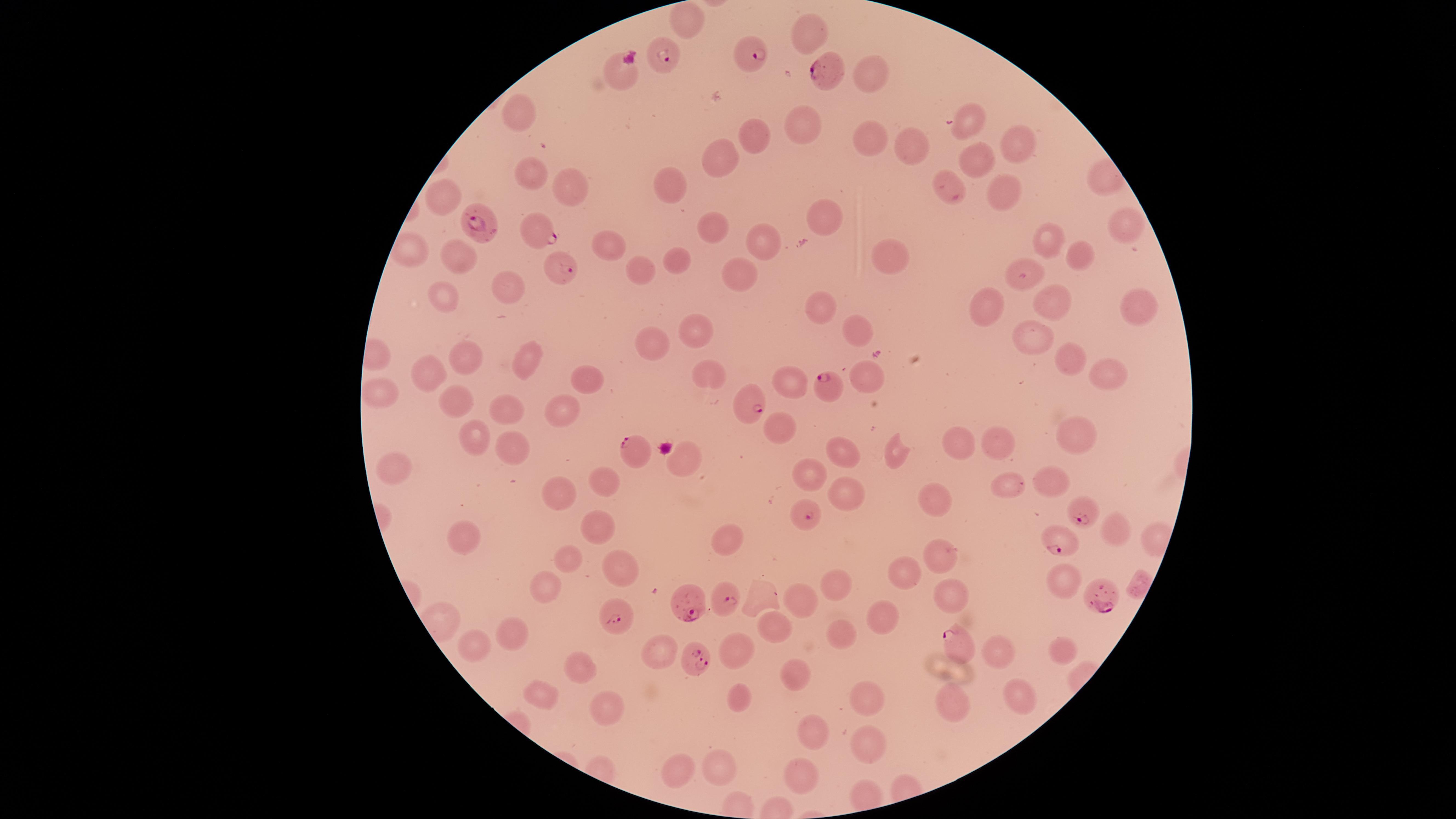

Approximate marker points as {x, y} in pixels.
Summary:
  - Parasitized red blood cells: {663, 54}, {753, 54}, {619, 72}, {830, 75}, {481, 223}, {537, 230}, {556, 264}, {827, 386}, {748, 403}, {633, 449}, {805, 515}, {1085, 515}, {1065, 540}, {692, 599}, {726, 600}, {1108, 601}, {619, 615}, {961, 640}, {694, 659}
  - Uninfected red blood cells: {682, 24}, {806, 34}, {868, 71}, {518, 116}, {806, 122}, {964, 123}, {760, 133}, {871, 139}, {1018, 140}, {914, 145}, {723, 156}, {976, 162}, {538, 173}, {571, 184}, {943, 185}, {673, 187}, {1004, 188}, {446, 196}, {827, 216}, {1123, 223}, {711, 224}, {762, 240}, {1044, 241}, {604, 246}, {459, 252}, {1080, 256}, {891, 261}, {672, 262}, {636, 273}, {738, 273}, {1029, 279}, {507, 288}, {446, 299}, {1135, 302}, {1052, 304}, {982, 310}, {818, 312}, {859, 325}, {701, 332}, {1034, 336}, {650, 346}, {472, 358}, {1070, 358}, {521, 361}, {1109, 366}, {871, 375}, {430, 376}, {588, 378}, {711, 378}, {783, 382}, {383, 393}, {452, 396}, {504, 407}, {560, 411}, {777, 427}, {478, 436}, {1075, 437}, {954, 441}, {995, 442}, {512, 449}, {899, 454}, {839, 455}, {687, 461}, {398, 469}, {815, 469}, {1052, 480}, {608, 481}, {1006, 486}, {558, 487}, {840, 500}, {932, 505}, {597, 528}, {1114, 530}, {466, 540}, {729, 541}, {570, 557}, {938, 561}, {619, 568}, {900, 573}, {546, 578}, {833, 583}, {1064, 583}, {949, 598}, {799, 599}, {877, 615}, {772, 622}, {519, 634}, {840, 634}, {474, 644}, {996, 646}, {1064, 648}, {657, 649}, {734, 652}, {574, 661}, {795, 677}, {1022, 690}, {738, 697}, {866, 698}, {541, 701}, {950, 705}, {604, 706}, {817, 732}, {869, 743}, {719, 766}, {800, 772}, {679, 774}
  - Species: Plasmodium falciparum
  - Image size: 1456×819 pixels
  - Capture: smartphone photograph through the microscope eyepiece
  - Stain: Giemsa
  - Preparation: thin smear of blood
  - Field of view: single
  - Presence: malaria parasites detected
  - Visible region: circular